Comment on the morphology of the red blood cells.
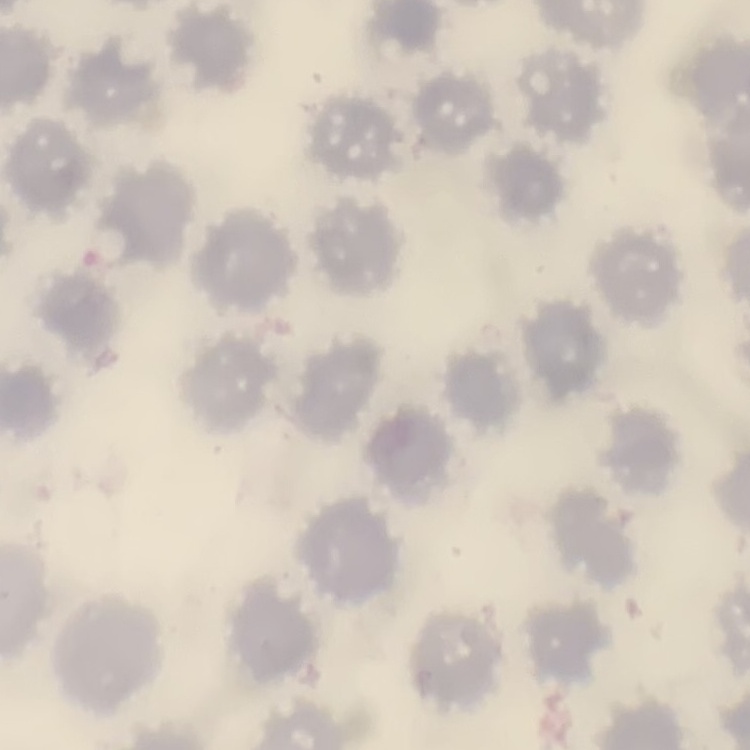

They show no rouleaux formation.

{
  "stain": "Field's or Giemsa",
  "preparation": "thin peripheral smear",
  "image_type": "one tile cut from a larger photomicrograph"
}